Give the extent of all uninfected red blood cells.
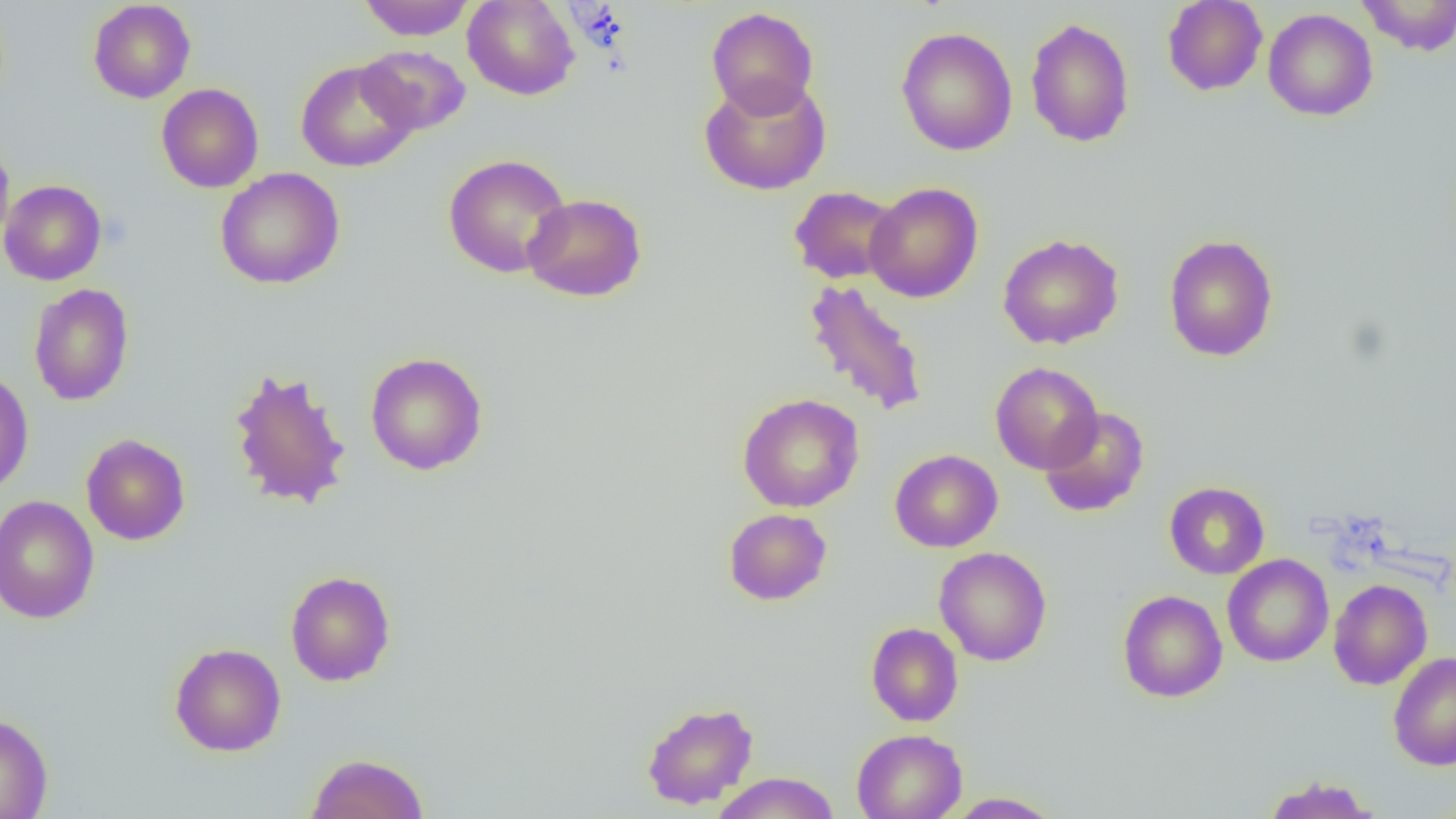

Approximate bounding boxes as (x1, y1, x2, y2) in pixels.
Uninfected red blood cells: (88, 0, 196, 103), (358, 0, 474, 41), (462, 0, 579, 100), (1162, 0, 1268, 96), (1356, 0, 1456, 55), (706, 6, 819, 117), (1263, 8, 1378, 121), (1025, 17, 1135, 147), (896, 26, 1018, 155), (357, 45, 470, 136), (296, 60, 418, 172), (699, 76, 831, 196), (156, 83, 264, 193), (0, 142, 15, 254), (443, 153, 571, 278), (215, 167, 345, 289), (0, 180, 106, 285), (865, 182, 984, 303), (788, 185, 902, 284), (522, 193, 647, 302), (997, 233, 1125, 350), (1164, 234, 1278, 362), (802, 279, 930, 418), (28, 283, 135, 406), (365, 352, 488, 475), (990, 362, 1103, 474), (228, 366, 352, 511), (0, 369, 34, 496), (737, 393, 864, 513), (1039, 407, 1150, 518), (81, 434, 191, 545), (889, 449, 1003, 552), (1164, 481, 1269, 579), (0, 495, 100, 624), (723, 508, 832, 606), (934, 546, 1052, 666), (1222, 554, 1334, 667), (285, 570, 396, 686), (1328, 579, 1433, 690), (1117, 590, 1228, 702), (866, 623, 963, 727), (169, 642, 286, 756), (1388, 650, 1456, 771), (641, 701, 759, 810), (0, 712, 53, 819), (852, 729, 966, 818), (306, 752, 429, 819), (709, 771, 841, 819), (1262, 775, 1380, 819), (946, 792, 1064, 818).

slide-level diagnosis = no evidence of blood parasites
preparation = thin blood smear
magnification = 1000x
modality = light microscopy
field of view = single
image size = 1456×819 pixels